Classify this cell by malaria status.
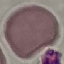

It is uninfected.

{
  "capture": "smartphone through the microscope eyepiece",
  "preparation": "thin blood smear",
  "stain": "Giemsa",
  "image_type": "cell patch, automatically extracted from a larger field of view and resized to 64 × 64 pixels"
}